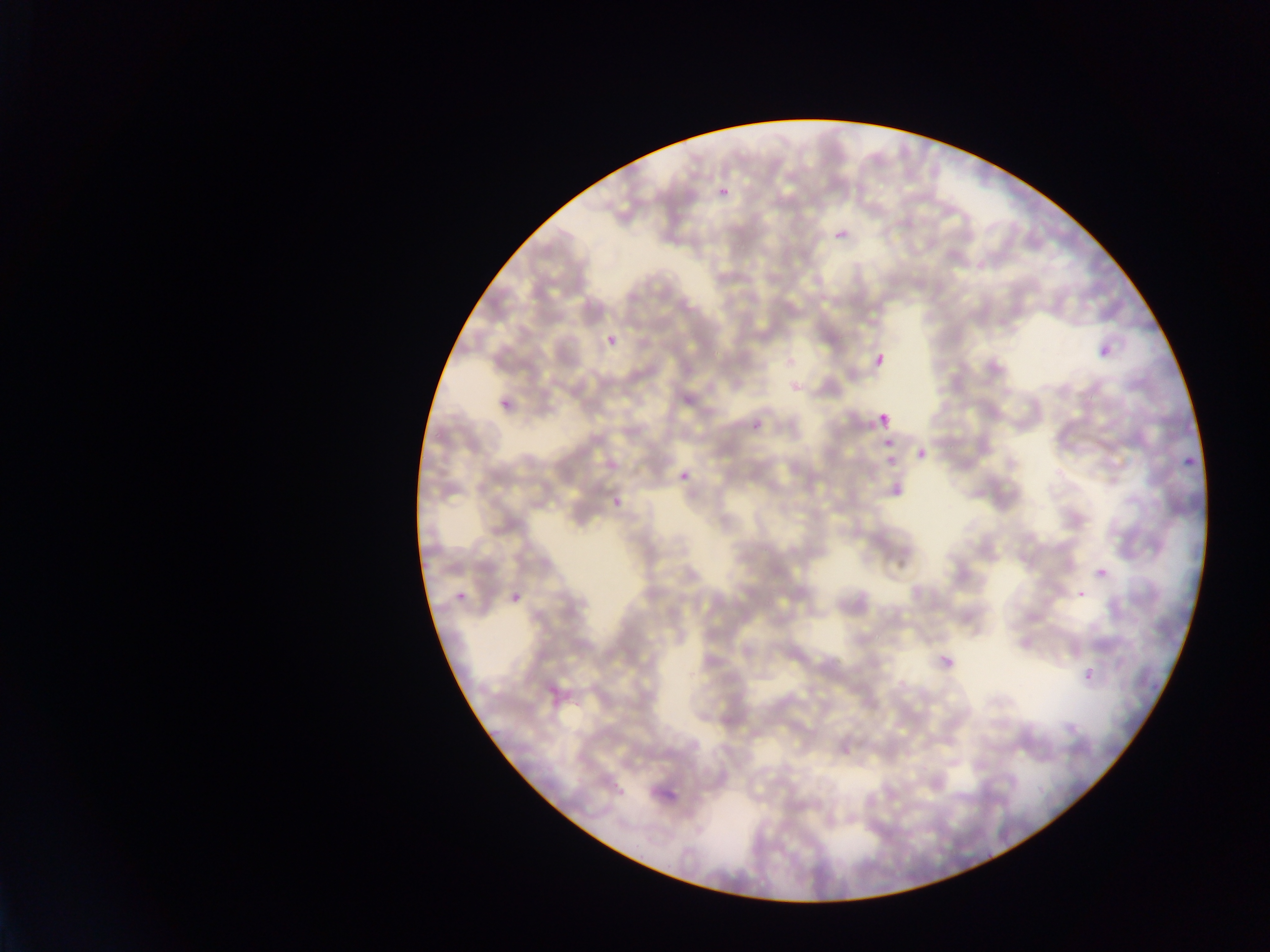

preparation = thin blood smear
image size = 1270×952 pixels
field of view = single
country = Ghana
Plasmodium parasite locations = approximate bounding boxes as left top right bottom in pixels: 716 182 733 193; 834 229 849 245; 606 334 619 348; 1093 341 1115 355; 870 349 892 373; 494 388 518 412; 875 410 895 432; 750 417 766 436; 868 437 905 454; 916 448 929 462; 883 457 905 473; 1177 457 1197 471; 679 470 693 485; 607 497 636 511; 1096 567 1109 581; 445 573 471 607; 1075 588 1088 601; 507 592 523 611; 934 645 963 678; 1081 667 1100 689
capture = mobile-phone photograph through a microscope